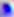
{
  "identification": "Toxoplasma gondii",
  "magnification": "400x",
  "modality": "micrograph"
}